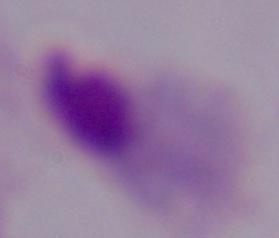

Micrograph. A trichomonad is shown. 1000x magnification.